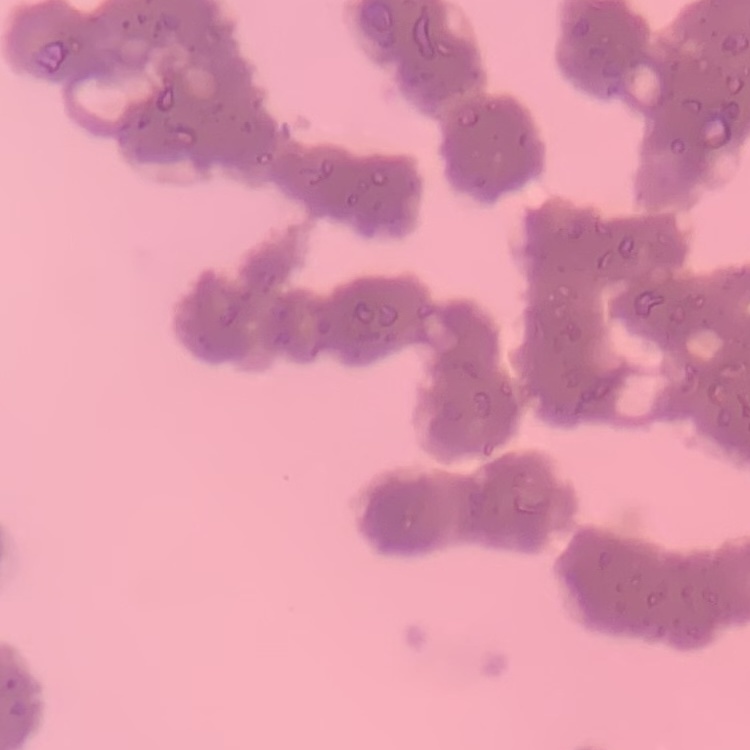
{
  "erythrocyte_morphology": "rouleaux formation",
  "preparation": "thin peripheral smear",
  "stain": "Field's or Giemsa",
  "image_type": "one tile cut from a larger photomicrograph"
}